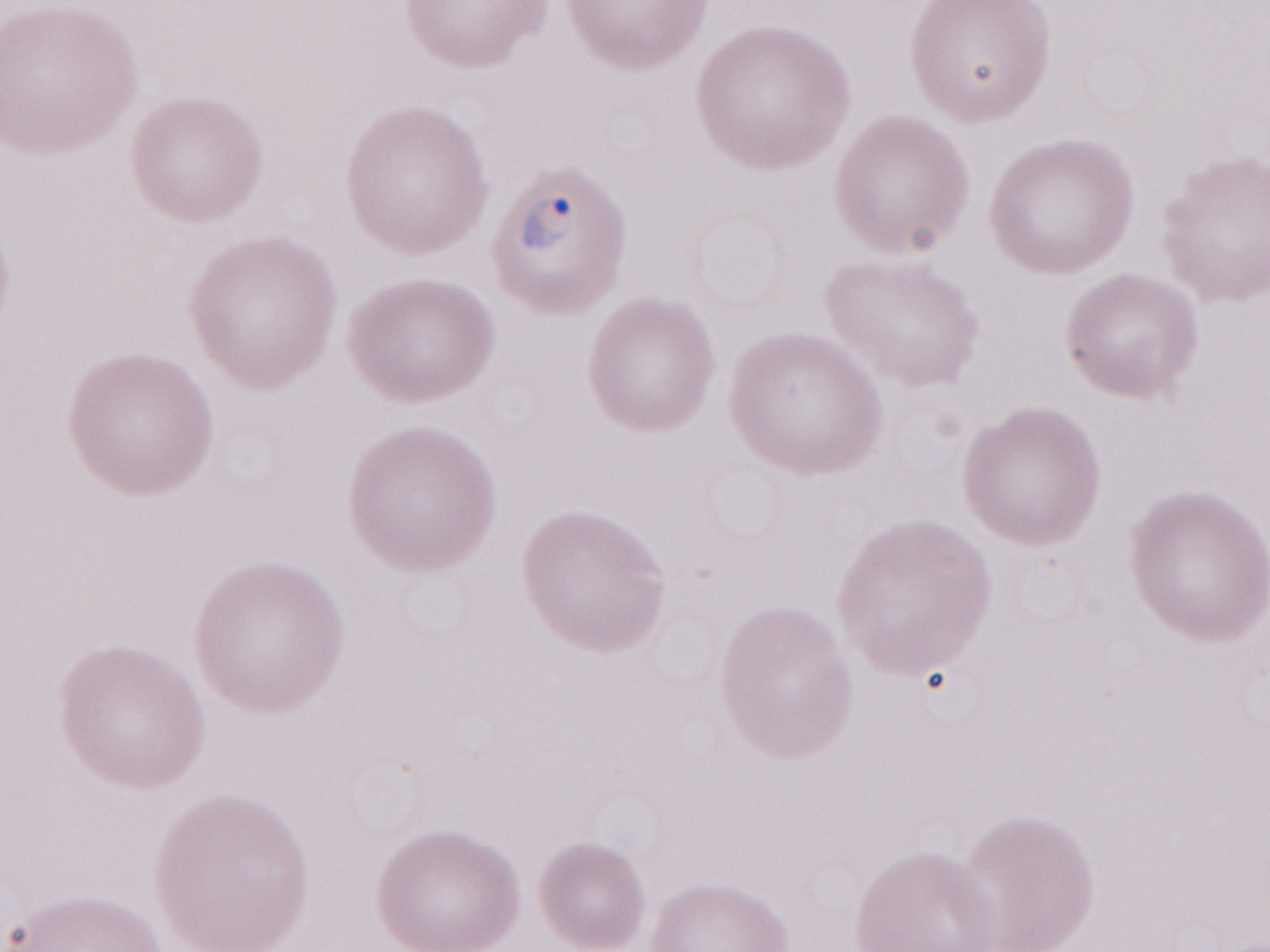
Single field of view. Thin peripheral-blood smear. Image is 1270×952 pixels. May-Grünwald-Giemsa (MGG) stain. Patient-level malaria diagnosis: positive. Olympus BX43 microscope, Olympus DP73 camera. 1,000x magnification.